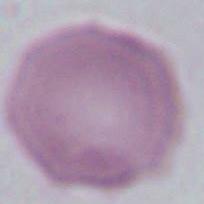
Micrograph. A red blood cell is seen. Captured at 1000x magnification.